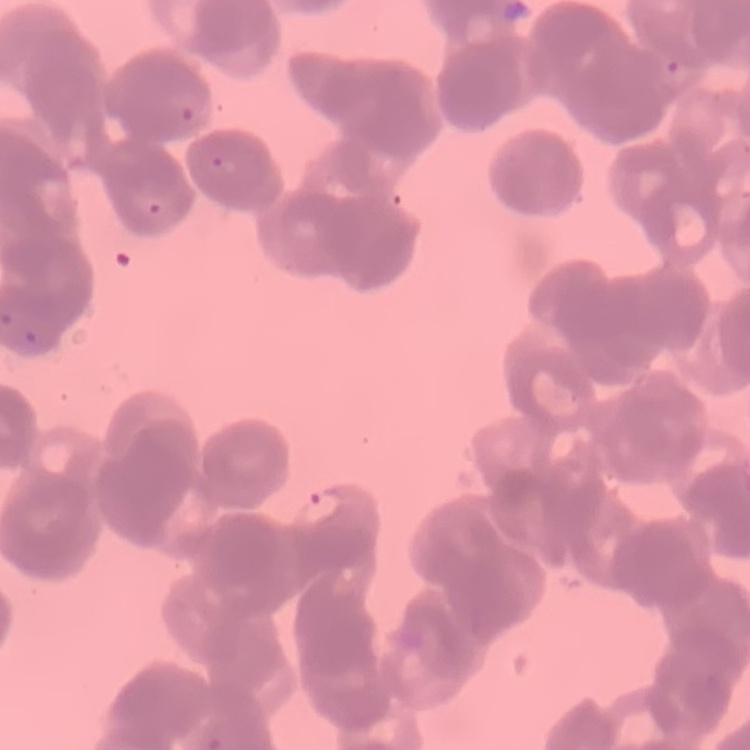 The erythrocytes exhibit rouleaux formation. Field's or Giemsa stain. Square crop of a larger photomicrograph. Thin peripheral smear.